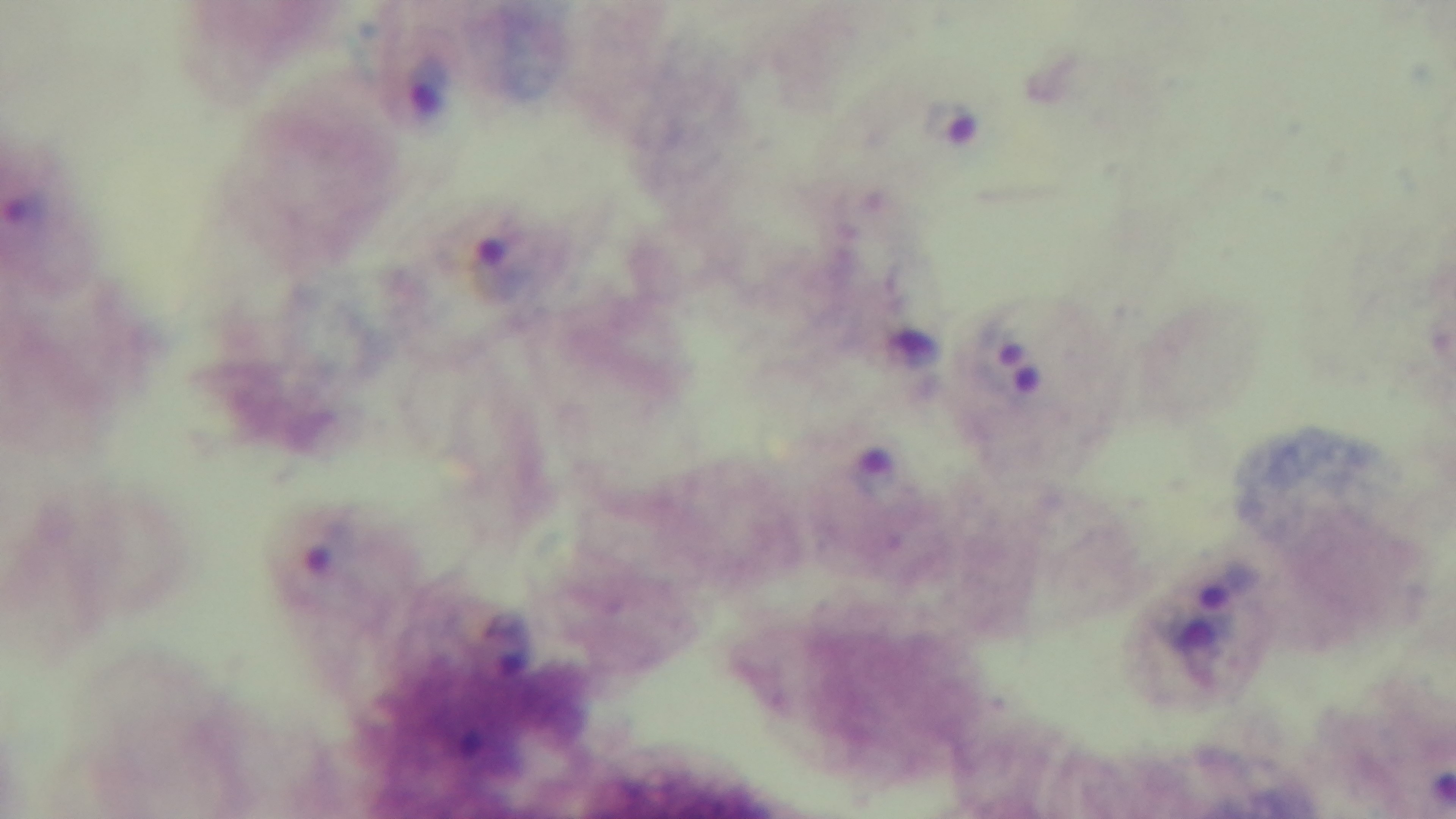
Preparation: thick smear. Mounted 4K digital camera. One field from the slide. 100x oil-immersion objective. Malaria status: positive. Giemsa stain. Light microscopy.